Name the parasite shown.
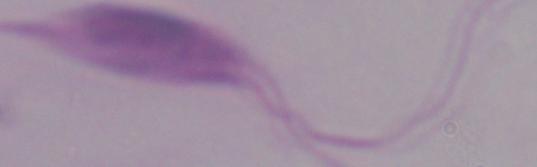

This is Leishmania.

magnification = 1000x
modality = micrograph